Report the malaria status of this cell.
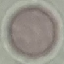

It is uninfected.

preparation = thin blood smear
stain = Giemsa
capture = smartphone through the microscope eyepiece
image type = cell patch, automatically extracted from a larger field of view and resized to 64 × 64 pixels